Give the position of every Plasmodium parasite visible.
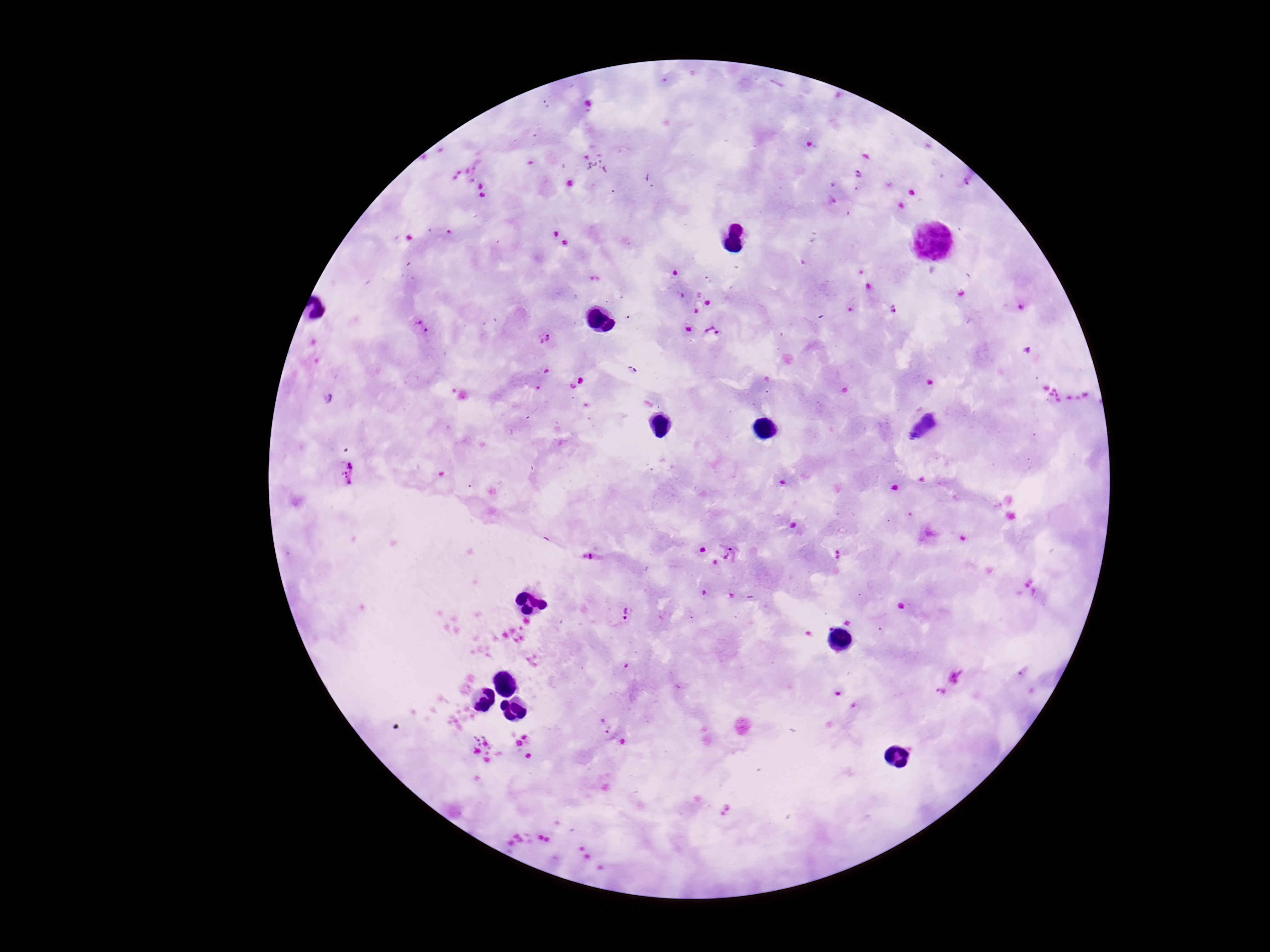
Approximate centers as [x, y] in pixels.
Plasmodium parasites: [857, 175], [893, 309], [420, 328], [713, 332], [545, 338], [581, 380], [572, 387], [343, 473], [587, 554], [729, 554], [622, 613], [942, 694].

Image is 1270×952 pixels. 100x magnification. One field from this slide. Patient malaria status: infected. Photographed through the microscope eyepiece with a smartphone camera. Thick blood smear. Giemsa-stained preparation.